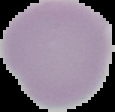
preparation: thin blood smear
image_type: cell region segmented out of the field of view; surrounding area masked to black
result: no malaria parasites seen
image_size: 115×112 pixels